Classify this cell by malaria status.
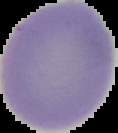
It is uninfected.

Summary:
  - Preparation: thin blood smear
  - Image size: 118×133 pixels
  - Image type: cell region segmented out of the field of view; surrounding area masked to black